Assess the morphology of the erythrocytes.
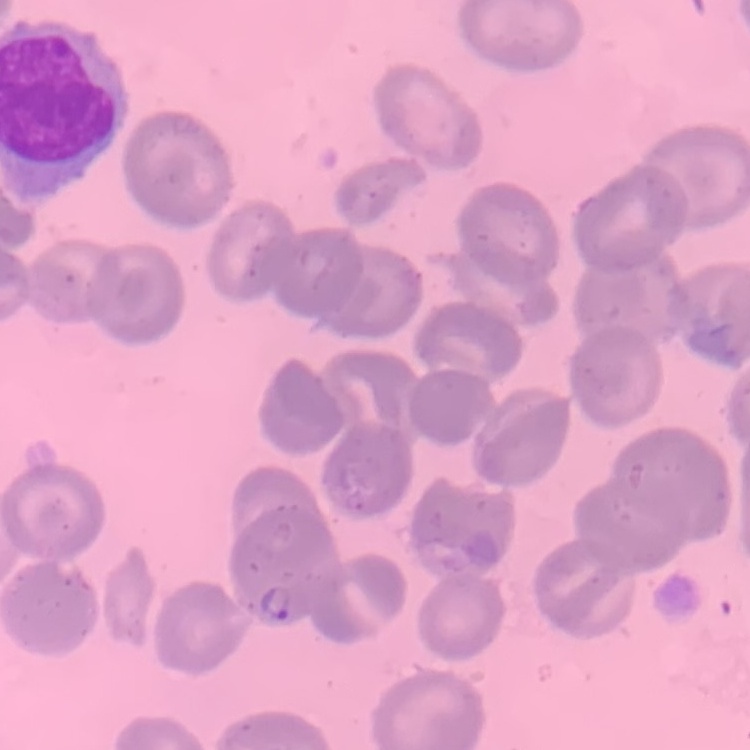
No rouleaux formation.

Square crop of a larger photomicrograph. Thin blood film. Stained with either Field's or Giemsa.